Name the parasite shown.
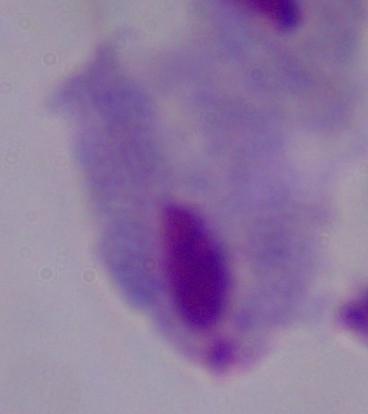

This is a trichomonad.

Summary:
  - Magnification: 1000x
  - Modality: micrograph